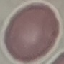
Summary:
  - Malaria status: uninfected
  - Image type: cell patch, automatically extracted from a larger field of view and resized to 64 × 64 pixels
  - Capture: smartphone camera at the microscope eyepiece
  - Stain: Giemsa
  - Preparation: thin blood smear